Identify the parasite.
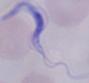

A trypanosome.

{
  "magnification": "1000x",
  "modality": "micrograph"
}